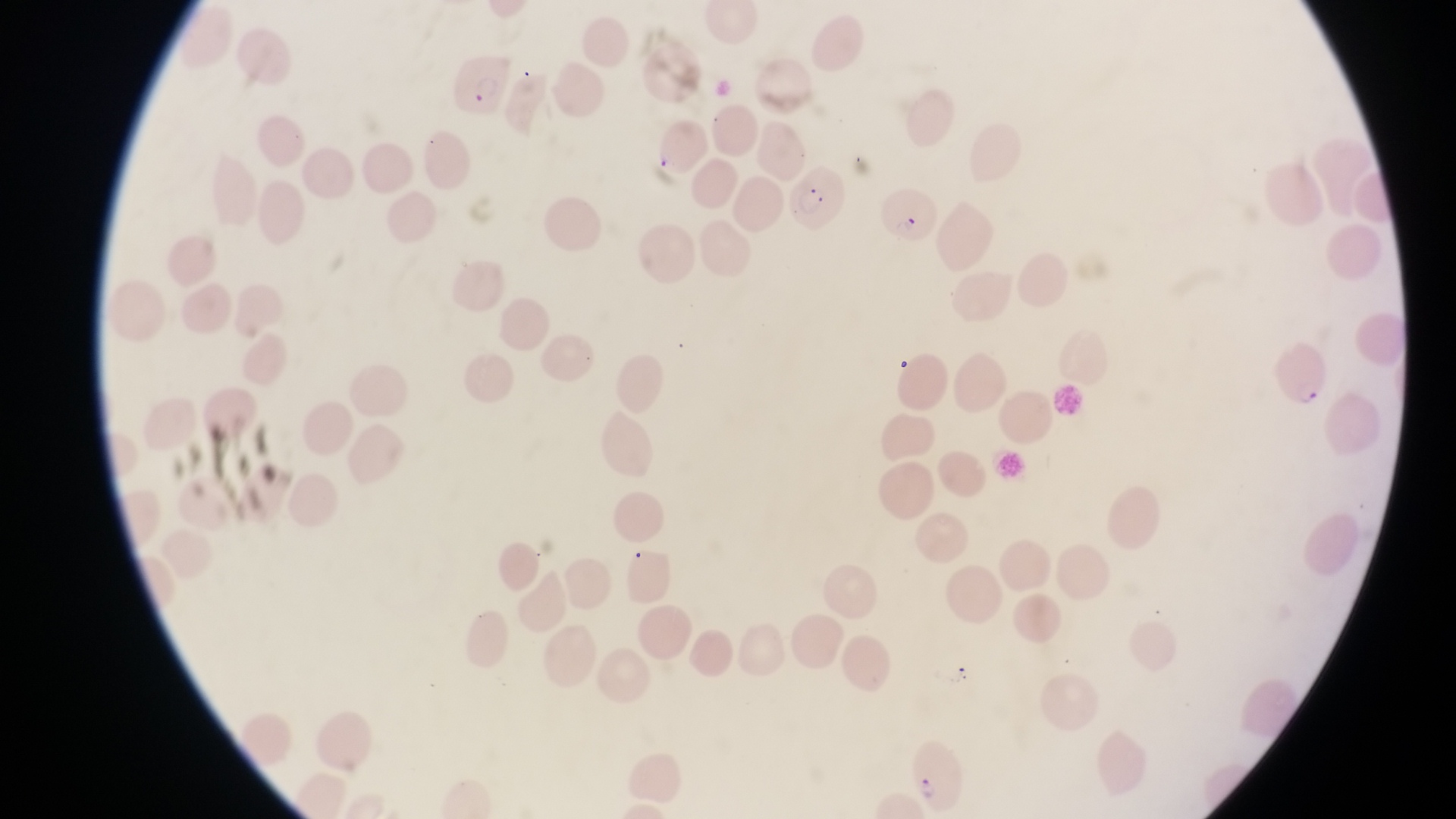 Approximate bounding boxes as left top right bottom in pixels. Parasitised red blood cell locations: 452 50 510 121; 783 159 841 219; 880 182 938 245; 1279 337 1328 411. At a magnification of 1000x. Captured by a smartphone held over the eyepiece of an Olympus CX-23 microscope. Sample from Uganda. Thin blood smear. Single field of view. Image is 1456×819 pixels.